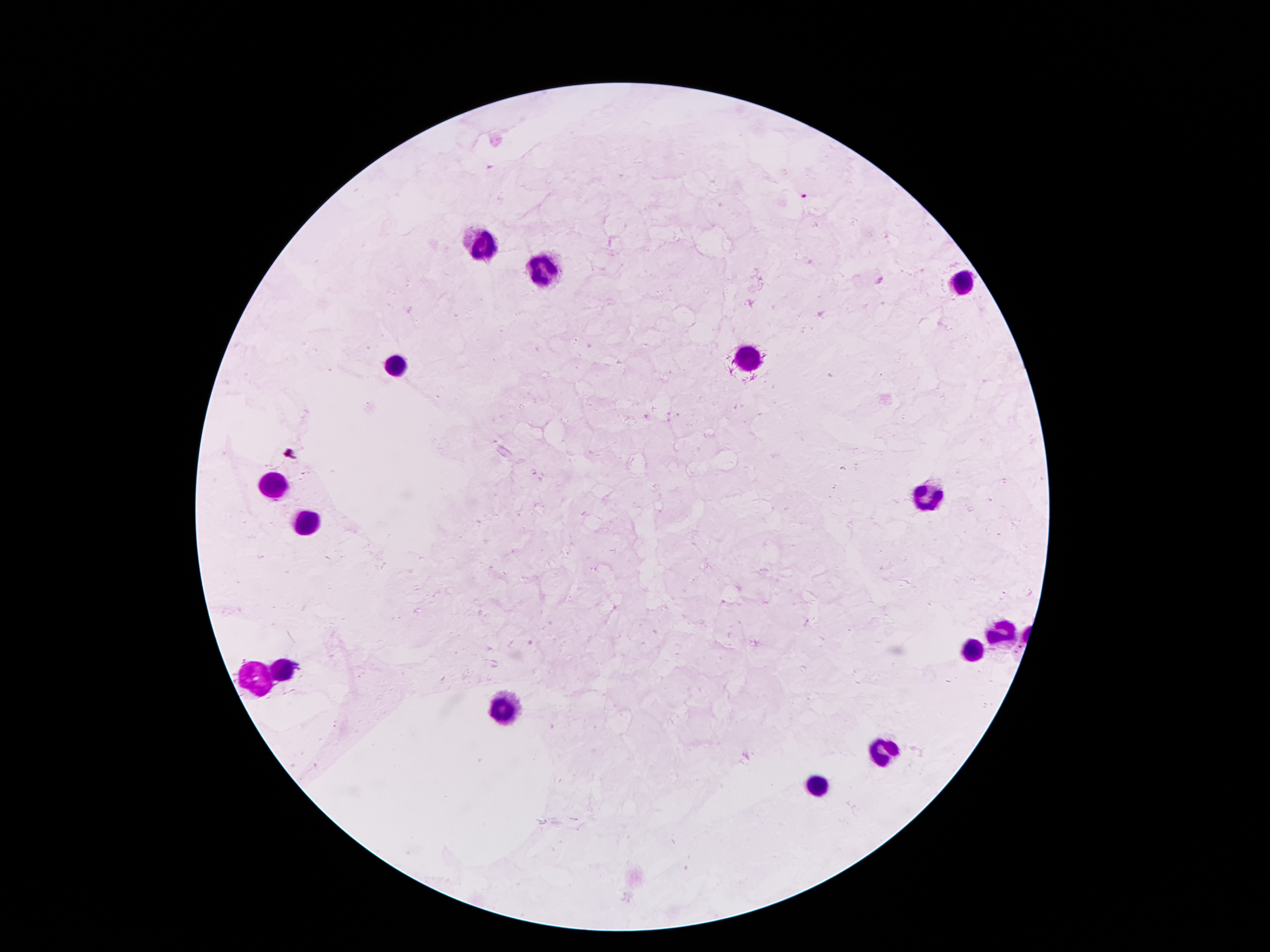
coordinate format = approximate centers as {x, y} in pixels
malaria parasite locations = {803, 197}
leukocyte locations = {482, 245}, {545, 270}, {961, 280}, {396, 359}, {747, 359}, {273, 486}, {930, 497}, {307, 522}, {1003, 631}, {971, 652}, {283, 672}, {256, 673}, {505, 708}, {882, 752}, {816, 785}
preparation = thick blood film
magnification = 100x
image size = 1270×952 pixels
field of view = single
patient malaria status = positive for Plasmodium falciparum
stain = Giemsa
capture = smartphone through the microscope eyepiece